Locate and identify every blood parasite.
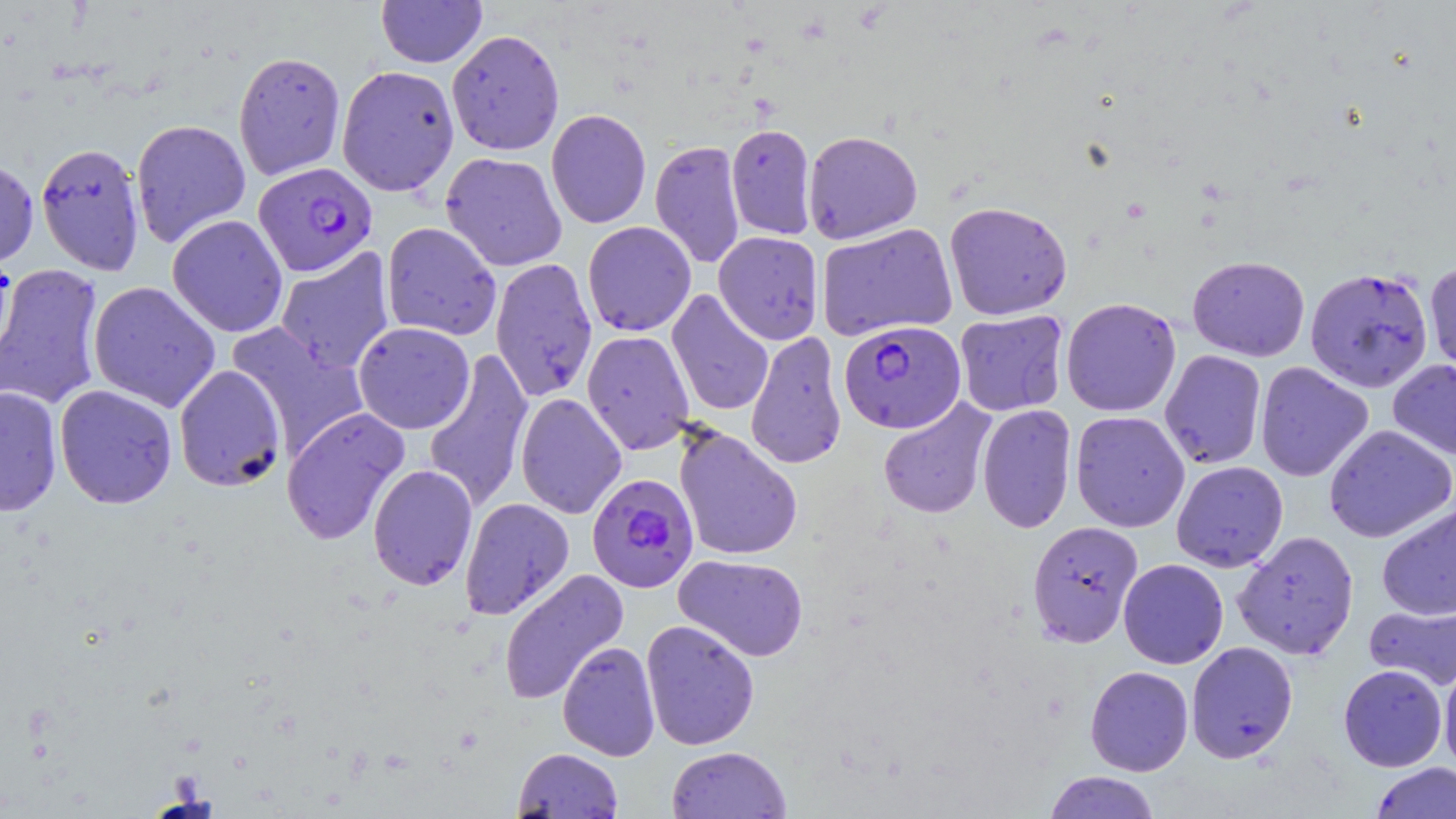

Approximate bounding boxes as named x1/y1/x2/y2 corners in pixels.
Plasmodium falciparum-infected red blood cells: (x1=253, y1=162, x2=378, y2=277), (x1=839, y1=319, x2=967, y2=434), (x1=586, y1=472, x2=700, y2=593).
No Plasmodium ovale, Plasmodium malariae, Plasmodium vivax, Babesia divergens, or Trypanosoma brucei observed.

slide_level_diagnosis: Plasmodium falciparum
uninfected_red_blood_cell_locations: 'approximate bounding boxes as named x1/y1/x2/y2 corners in pixels: (x1=376, y1=0, x2=487, y2=67), (x1=446, y1=29, x2=565, y2=156), (x1=233, y1=51, x2=346, y2=180), (x1=336, y1=65, x2=459, y2=197), (x1=546, y1=109, x2=651, y2=229), (x1=131, y1=118, x2=251, y2=248), (x1=726, y1=123, x2=817, y2=240), (x1=803, y1=130, x2=923, y2=244), (x1=650, y1=140, x2=746, y2=269), (x1=35, y1=141, x2=146, y2=276), (x1=441, y1=152, x2=567, y2=271), (x1=0, y1=157, x2=39, y2=271), (x1=944, y1=201, x2=1072, y2=320), (x1=167, y1=214, x2=288, y2=338), (x1=582, y1=221, x2=696, y2=336), (x1=381, y1=222, x2=502, y2=341), (x1=816, y1=223, x2=958, y2=341), (x1=713, y1=231, x2=824, y2=345), (x1=274, y1=247, x2=396, y2=374), (x1=0, y1=250, x2=16, y2=368), (x1=1187, y1=255, x2=1310, y2=361), (x1=490, y1=258, x2=599, y2=402), (x1=1424, y1=260, x2=1456, y2=381), (x1=0, y1=263, x2=105, y2=410), (x1=1305, y1=266, x2=1434, y2=393), (x1=88, y1=281, x2=221, y2=412), (x1=666, y1=289, x2=774, y2=417), (x1=1060, y1=297, x2=1181, y2=417), (x1=954, y1=309, x2=1070, y2=417), (x1=353, y1=321, x2=475, y2=434), (x1=227, y1=322, x2=369, y2=458), (x1=582, y1=330, x2=694, y2=455), (x1=745, y1=331, x2=847, y2=470), (x1=422, y1=348, x2=534, y2=514), (x1=1159, y1=349, x2=1267, y2=469), (x1=1388, y1=359, x2=1456, y2=461), (x1=1255, y1=361, x2=1373, y2=482), (x1=173, y1=364, x2=288, y2=492), (x1=54, y1=385, x2=177, y2=509), (x1=0, y1=386, x2=63, y2=517), (x1=515, y1=393, x2=628, y2=519), (x1=878, y1=398, x2=996, y2=519), (x1=976, y1=403, x2=1077, y2=534), (x1=281, y1=407, x2=411, y2=545), (x1=1070, y1=410, x2=1190, y2=532), (x1=1323, y1=424, x2=1456, y2=543), (x1=674, y1=425, x2=803, y2=562), (x1=1171, y1=460, x2=1288, y2=572), (x1=368, y1=464, x2=478, y2=591), (x1=459, y1=497, x2=575, y2=620), (x1=1377, y1=503, x2=1456, y2=621), (x1=1027, y1=520, x2=1144, y2=647), (x1=1233, y1=530, x2=1359, y2=659), (x1=673, y1=554, x2=809, y2=662), (x1=1118, y1=558, x2=1228, y2=669), (x1=499, y1=568, x2=629, y2=705), (x1=1364, y1=600, x2=1456, y2=691), (x1=641, y1=619, x2=760, y2=750), (x1=557, y1=641, x2=661, y2=761), (x1=1186, y1=641, x2=1298, y2=763), (x1=1439, y1=657, x2=1456, y2=776), (x1=1338, y1=664, x2=1448, y2=772), (x1=1085, y1=666, x2=1193, y2=776), (x1=666, y1=745, x2=792, y2=818), (x1=512, y1=747, x2=623, y2=818), (x1=1371, y1=762, x2=1456, y2=819), (x1=1043, y1=771, x2=1161, y2=819)'
magnification: 1000x
field_of_view: one of a larger specimen
preparation: thin blood film
image_size: 1456×819 pixels
modality: light microscopy
stain: May-Grünwald-Giemsa